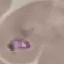
Malaria status: parasitized. Acquired by smartphone through the microscope eyepiece. Thin blood film. Automatically extracted cell patch, resized to 64 × 64 pixels. Giemsa-stained preparation.